Evaluate for malaria.
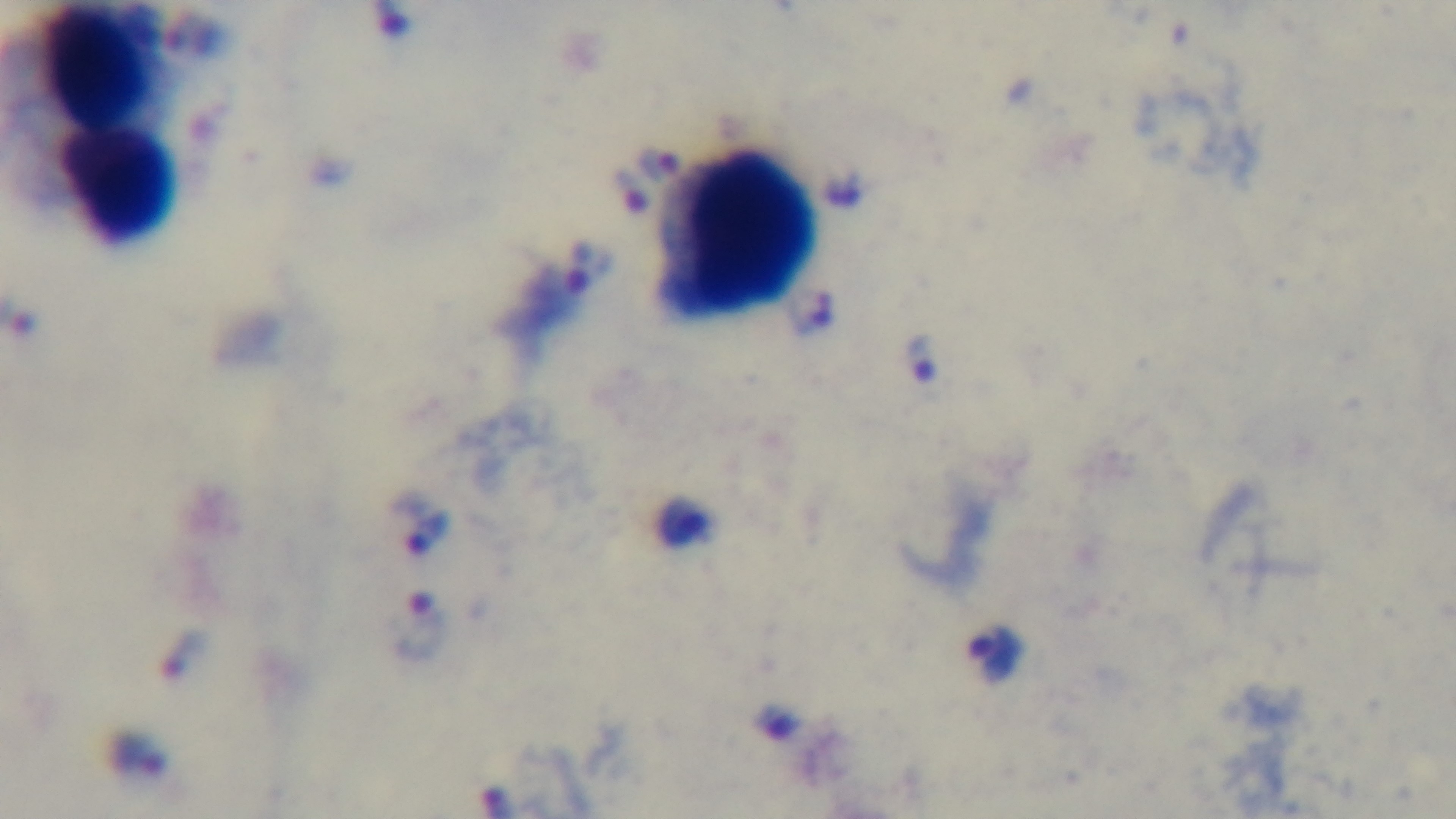
Infected.

Mounted 4K digital camera. Single field of view. Giemsa stain. Light microscopy. 100x oil-immersion objective. Preparation: thick.